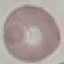

Summary:
  - Result: no malaria parasites detected
  - Capture: smartphone through the microscope eyepiece
  - Image type: cell patch, automatically extracted from a larger field of view and resized to 64 × 64 pixels
  - Preparation: thin blood film
  - Stain: Giemsa